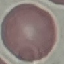
malaria status = uninfected
image type = cell patch, automatically extracted from a larger field of view and resized to 64 × 64 pixels
capture = smartphone camera at the microscope eyepiece
stain = Giemsa
preparation = thin smear